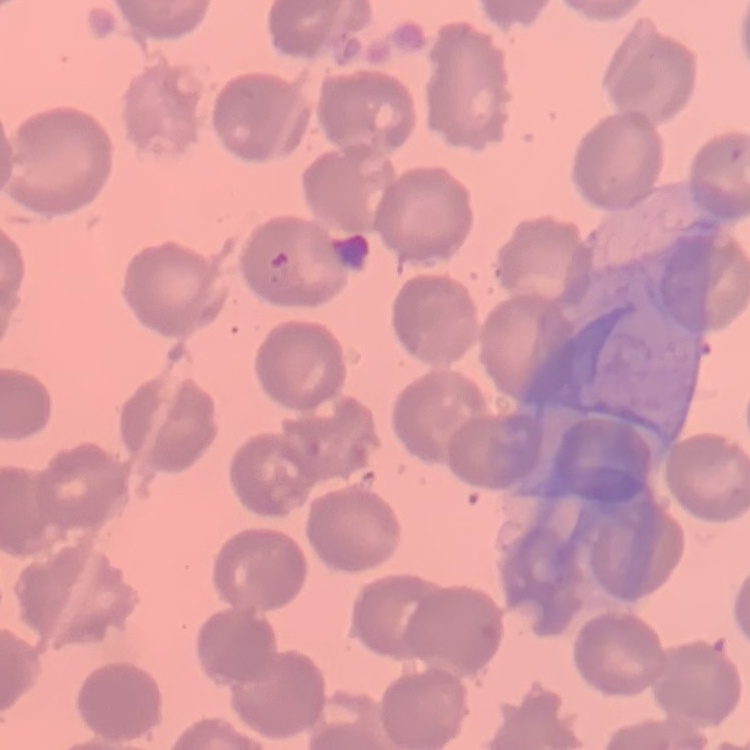 The red blood cells exhibit no rouleaux formation. One tile cut from a larger photomicrograph. Stained with either Field's or Giemsa. Thin blood film.